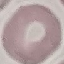
result = negative for malaria parasites
capture = smartphone through the microscope eyepiece
stain = Giemsa
image type = automatically extracted cell patch, resized to 64 × 64 pixels
preparation = thin smear